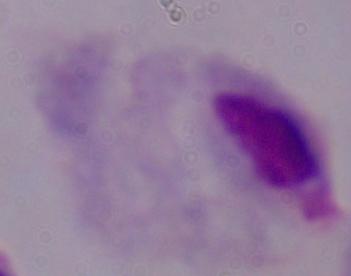

Summary:
  - Magnification: 1000x
  - Identification: trichomonad
  - Modality: photomicrograph